State which parasite is depicted.
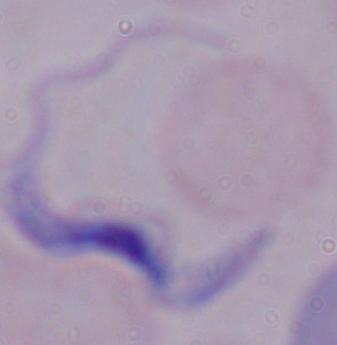

This is a trypanosome.

magnification: 1000x
modality: photomicrograph